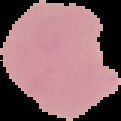

malaria status = uninfected
image size = 121×121 pixels
image type = segmented cell region with the area outside set to black
preparation = thin blood film